Describe the morphology of the erythrocytes.
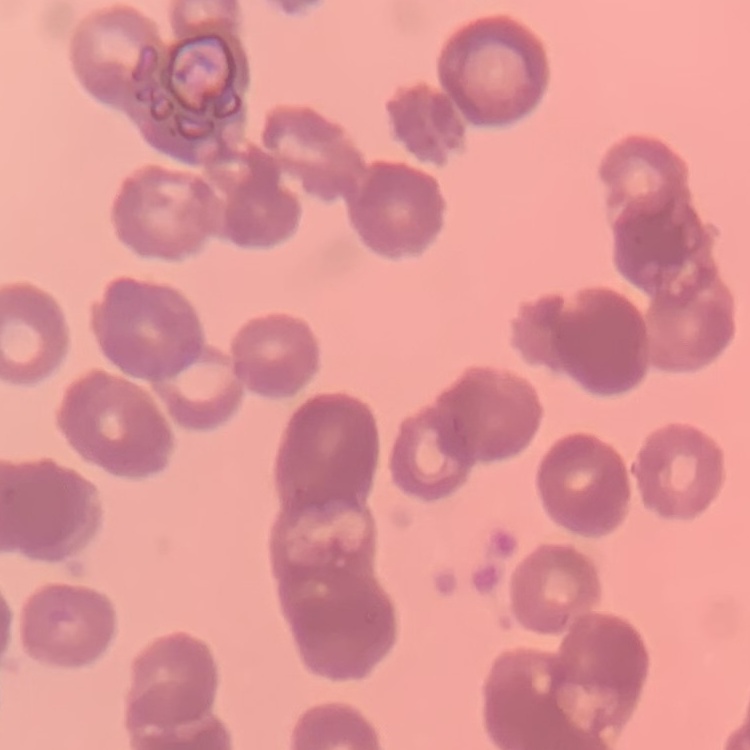

Rouleaux formation.

Field's or Giemsa stain. One tile cut from a larger photomicrograph. Thin blood smear.